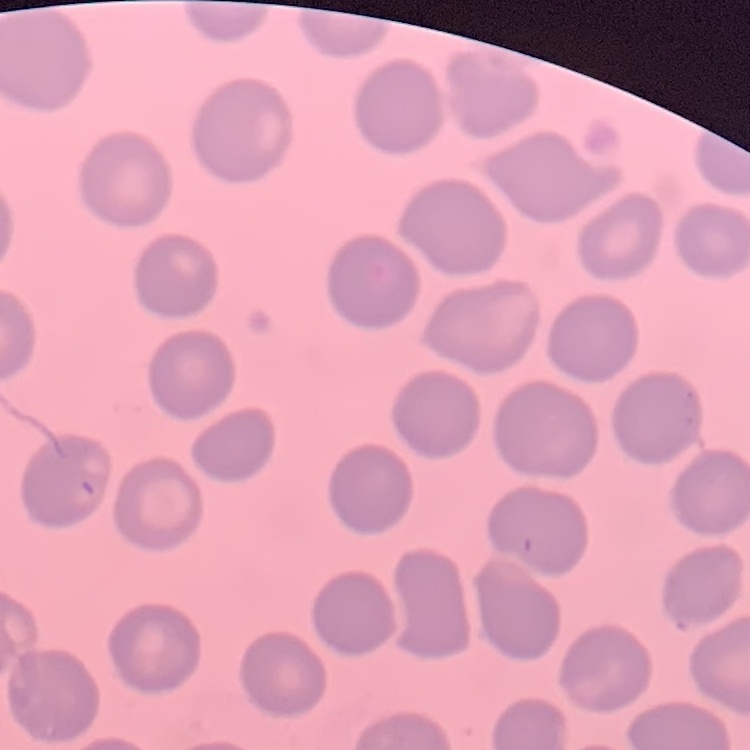
The erythrocytes exhibit no rouleaux formation. Square crop of a larger photomicrograph. Thin peripheral smear. Field's or Giemsa stain.